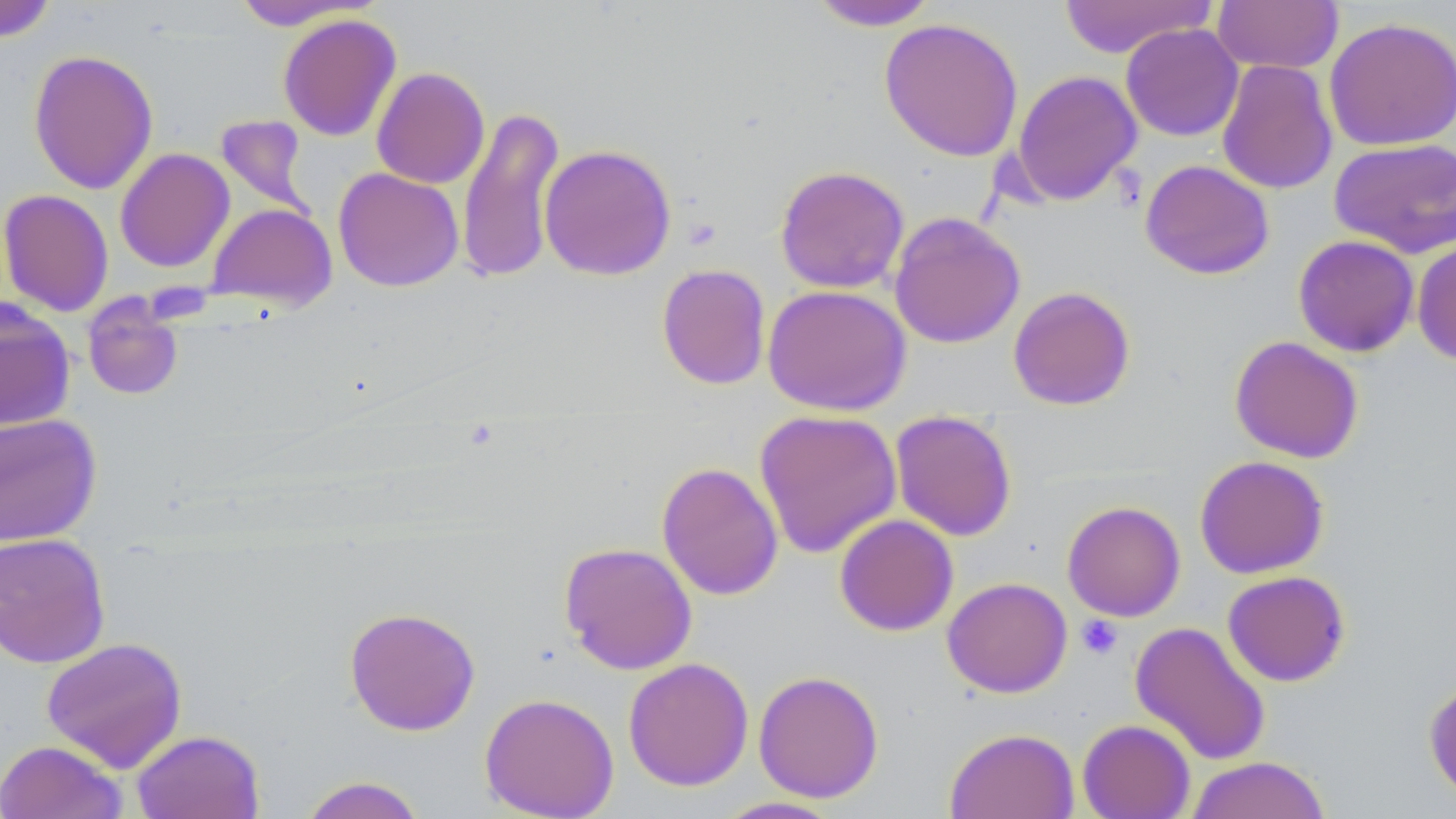
Approximate bounding boxes as (x1,y1)-(x2,y2) corner pairs in pixels. Uninfected red blood cell locations: (808,0)-(941,31), (1058,0)-(1214,58), (0,1)-(59,42), (230,1)-(374,30), (1212,1)-(1343,74), (277,13)-(401,141), (1323,16)-(1456,151), (879,17)-(1023,161), (1120,23)-(1244,142), (28,49)-(159,194), (1216,59)-(1338,195), (371,67)-(490,189), (1011,69)-(1143,207), (456,105)-(566,285), (215,114)-(316,220), (1328,137)-(1456,259), (538,143)-(677,281), (115,147)-(235,273), (1140,159)-(1275,280), (775,165)-(909,293), (333,167)-(464,292), (0,189)-(114,317), (206,203)-(337,310), (888,211)-(1026,349), (1293,235)-(1419,357), (1411,239)-(1456,366), (656,264)-(771,390), (762,284)-(911,415), (1007,285)-(1135,410), (82,295)-(184,400), (0,300)-(76,431), (1229,335)-(1364,463), (753,409)-(903,559), (890,411)-(1017,541), (0,413)-(102,546), (1194,454)-(1330,579), (656,461)-(784,601), (1062,501)-(1185,621), (834,514)-(959,636), (0,532)-(111,669), (559,541)-(697,675), (1222,570)-(1351,687), (942,576)-(1072,698), (343,606)-(481,736), (1129,620)-(1271,766), (41,637)-(188,772), (623,657)-(754,791), (753,670)-(884,803), (1423,678)-(1456,805), (479,692)-(619,819), (1077,719)-(1195,819), (944,727)-(1080,819), (131,729)-(265,819), (0,740)-(128,819), (1186,756)-(1331,818), (297,775)-(427,819), (710,795)-(849,818). Platelet locations: (1076,615)-(1123,659). Slide-level diagnosis: negative for blood parasites. Image is 1456×819 pixels. Thin blood film. Light microscopy. Single field of view. Captured at 1000x magnification. May-Grünwald-Giemsa-stained preparation.